Assess for Plasmodium parasites.
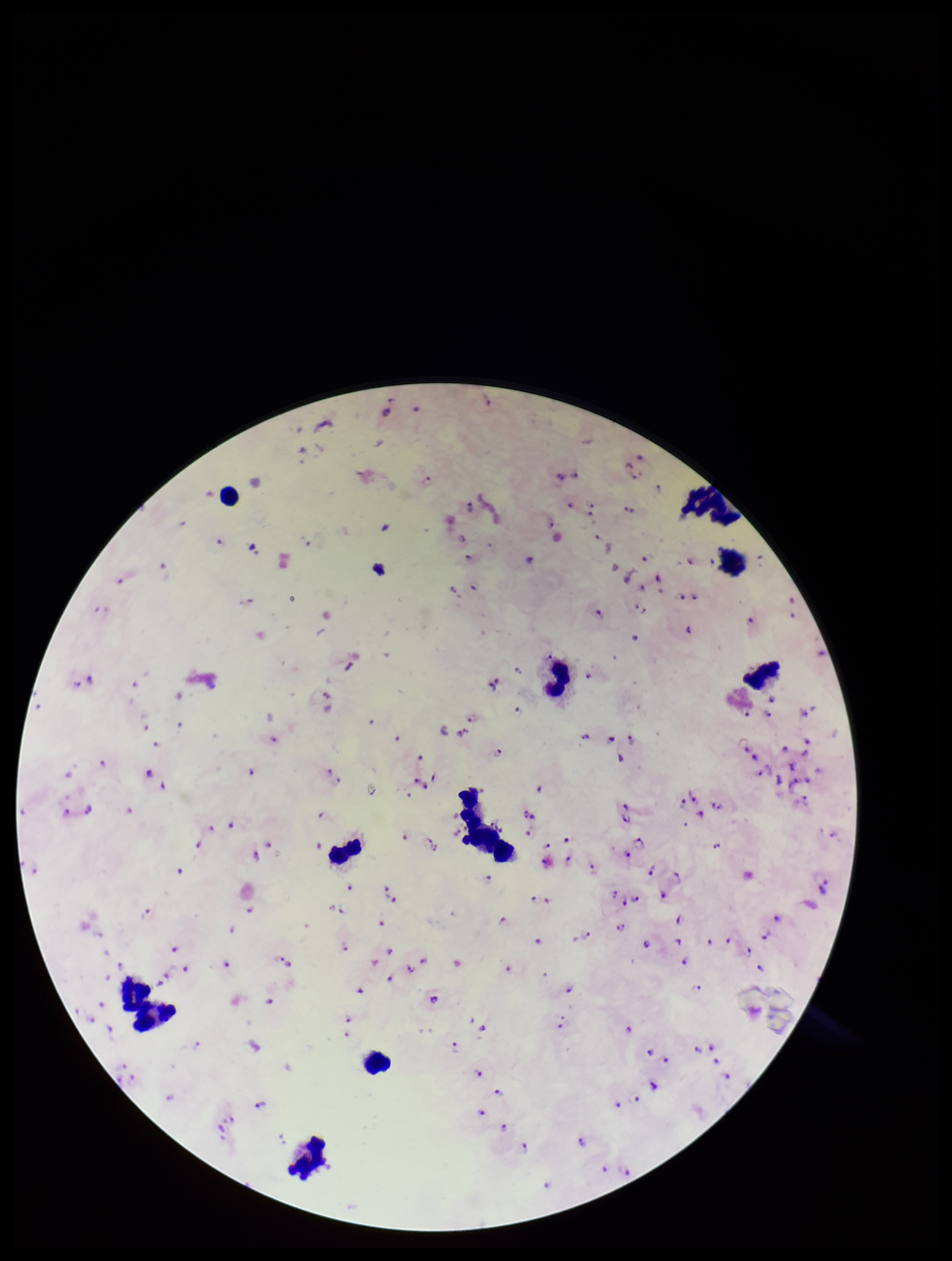

Detected.

Smartphone photograph taken through the eyepiece of a microscope. Patient malaria status: positive. Parasite count: 116. Image is 952×1261 pixels. Single field of view. Species reported for this patient: Plasmodium falciparum. Preparation: thick. Leukocyte count: 11. Stained with Giemsa.